Classify this cell by malaria status.
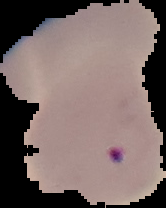
Parasitized.

{
  "image_size": "166×208 pixels",
  "image_type": "segmented cell region on a black background",
  "preparation": "thin blood smear"
}